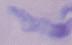
{
  "modality": "micrograph",
  "identification": "trypanosome",
  "magnification": "1000x"
}